Locate every blood parasite and identify its species.
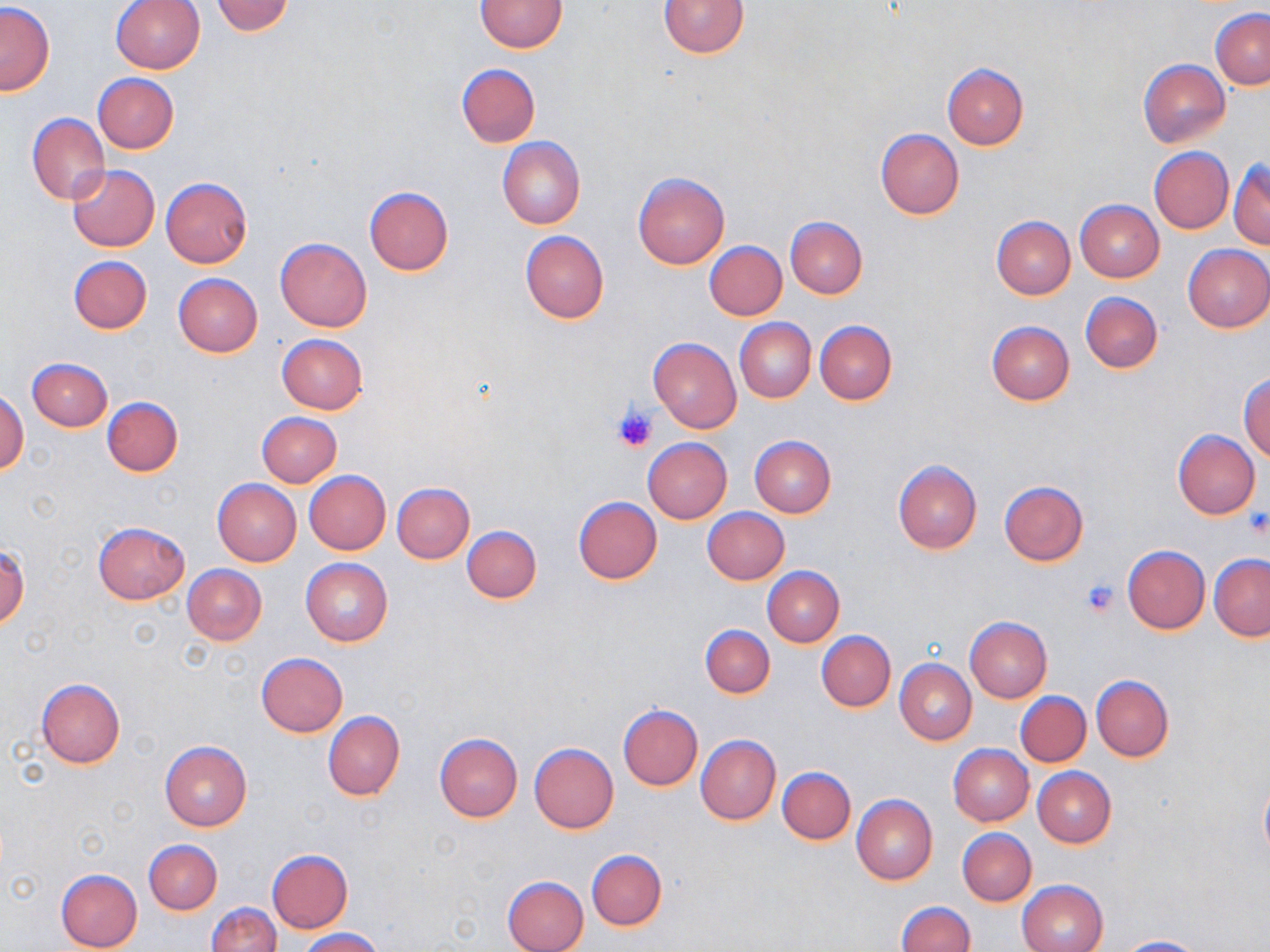

No blood parasites seen.

slide-level diagnosis = no evidence of blood parasites
modality = optical microscopy
stain = May-Grünwald-Giemsa
image size = 1270×952 pixels
field of view = one of a larger specimen
uninfected red blood cell locations = approximate bounding boxes as named x1/y1/x2/y2 corners in pixels: (x1=210, y1=0, x2=295, y2=36), (x1=475, y1=0, x2=568, y2=52), (x1=658, y1=0, x2=749, y2=57), (x1=110, y1=1, x2=205, y2=74), (x1=1, y1=3, x2=54, y2=96), (x1=1212, y1=9, x2=1270, y2=89), (x1=1139, y1=58, x2=1230, y2=148), (x1=455, y1=63, x2=540, y2=147), (x1=942, y1=64, x2=1029, y2=149), (x1=91, y1=73, x2=179, y2=152), (x1=27, y1=114, x2=110, y2=203), (x1=875, y1=128, x2=964, y2=219), (x1=498, y1=138, x2=585, y2=229), (x1=1149, y1=148, x2=1234, y2=233), (x1=1230, y1=161, x2=1269, y2=250), (x1=67, y1=164, x2=159, y2=251), (x1=633, y1=172, x2=729, y2=268), (x1=161, y1=177, x2=252, y2=267), (x1=364, y1=187, x2=453, y2=276), (x1=1074, y1=200, x2=1164, y2=281), (x1=991, y1=216, x2=1075, y2=299), (x1=787, y1=217, x2=867, y2=299), (x1=519, y1=231, x2=610, y2=323), (x1=275, y1=237, x2=372, y2=332), (x1=704, y1=241, x2=787, y2=320), (x1=1183, y1=244, x2=1270, y2=332), (x1=68, y1=256, x2=152, y2=335), (x1=173, y1=273, x2=263, y2=356), (x1=1080, y1=292, x2=1163, y2=374), (x1=734, y1=318, x2=815, y2=403), (x1=814, y1=320, x2=896, y2=405), (x1=986, y1=320, x2=1075, y2=405), (x1=276, y1=334, x2=368, y2=414), (x1=648, y1=337, x2=741, y2=432), (x1=27, y1=357, x2=112, y2=431), (x1=1239, y1=372, x2=1269, y2=462), (x1=0, y1=391, x2=29, y2=475), (x1=102, y1=398, x2=182, y2=476), (x1=257, y1=413, x2=341, y2=487), (x1=1172, y1=429, x2=1261, y2=519), (x1=749, y1=436, x2=836, y2=517), (x1=643, y1=438, x2=731, y2=523), (x1=892, y1=460, x2=982, y2=553), (x1=305, y1=471, x2=391, y2=555), (x1=212, y1=479, x2=301, y2=566), (x1=999, y1=480, x2=1088, y2=566), (x1=392, y1=482, x2=473, y2=563), (x1=574, y1=496, x2=662, y2=583), (x1=702, y1=507, x2=790, y2=584), (x1=92, y1=521, x2=190, y2=604), (x1=463, y1=526, x2=543, y2=603), (x1=0, y1=545, x2=29, y2=630), (x1=1121, y1=545, x2=1210, y2=634), (x1=1209, y1=554, x2=1270, y2=641), (x1=300, y1=558, x2=393, y2=646), (x1=183, y1=565, x2=266, y2=646), (x1=763, y1=567, x2=844, y2=647), (x1=964, y1=616, x2=1053, y2=702), (x1=701, y1=625, x2=774, y2=698), (x1=817, y1=631, x2=896, y2=712), (x1=256, y1=653, x2=348, y2=737), (x1=895, y1=659, x2=976, y2=744), (x1=1090, y1=675, x2=1172, y2=762), (x1=36, y1=679, x2=126, y2=768), (x1=1016, y1=692, x2=1090, y2=767), (x1=618, y1=704, x2=703, y2=791), (x1=322, y1=712, x2=404, y2=801), (x1=434, y1=733, x2=522, y2=821), (x1=695, y1=735, x2=781, y2=825), (x1=159, y1=741, x2=253, y2=831), (x1=529, y1=744, x2=619, y2=833), (x1=948, y1=745, x2=1033, y2=826), (x1=777, y1=766, x2=856, y2=844), (x1=1033, y1=767, x2=1116, y2=848), (x1=1259, y1=773, x2=1270, y2=864), (x1=851, y1=794, x2=937, y2=885), (x1=957, y1=828, x2=1037, y2=906), (x1=144, y1=839, x2=222, y2=915), (x1=265, y1=849, x2=354, y2=933), (x1=587, y1=850, x2=667, y2=930), (x1=55, y1=868, x2=143, y2=952), (x1=502, y1=875, x2=589, y2=952), (x1=1017, y1=879, x2=1109, y2=952), (x1=895, y1=901, x2=975, y2=952), (x1=207, y1=902, x2=280, y2=952), (x1=297, y1=927, x2=384, y2=952), (x1=1117, y1=935, x2=1211, y2=952)
platelet locations = approximate bounding boxes as named x1/y1/x2/y2 corners in pixels: (x1=612, y1=404, x2=658, y2=454), (x1=1243, y1=507, x2=1269, y2=540), (x1=1079, y1=577, x2=1120, y2=618)
preparation = thin blood smear
magnification = 1000x